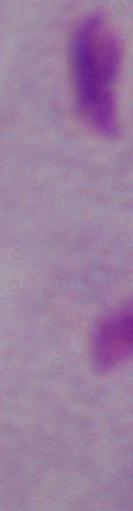
Summary:
  - Identification: trichomonad
  - Magnification: 1000x
  - Modality: micrograph